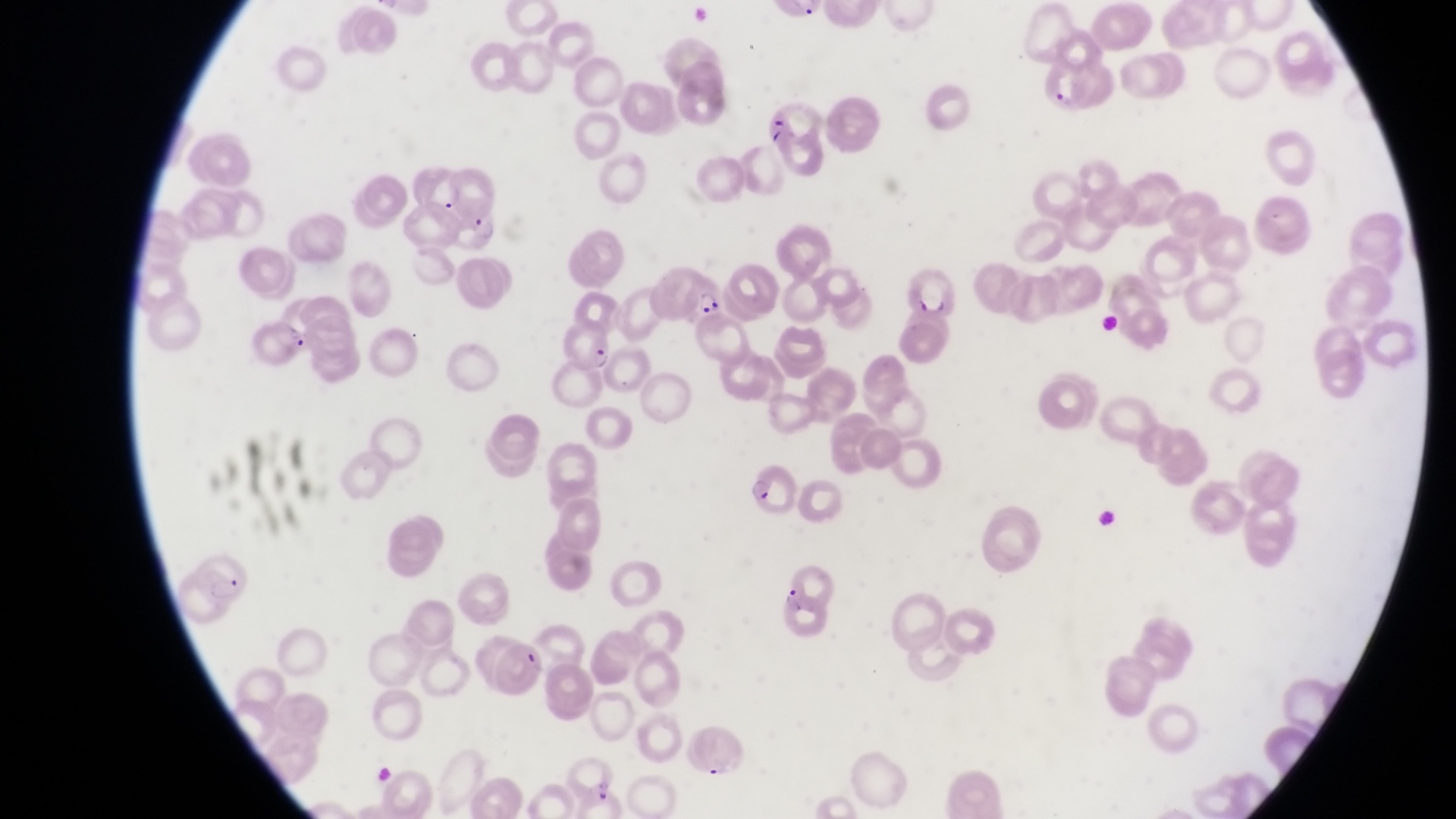 Approximate bounding boxes as {left, top, right, bottom} in pixels. Parasitised red blood cell locations: {444, 202, 504, 254}, {661, 262, 725, 320}, {901, 264, 960, 316}, {253, 312, 313, 365}, {561, 320, 617, 375}, {748, 462, 797, 520}, {184, 544, 261, 610}, {777, 582, 830, 641}, {682, 724, 750, 778}. Collected in Uganda. Image is 1456×819 pixels. Photographed through the eyepiece of an Olympus CX-23 microscope with a smartphone camera. Single field of view. Magnification of 1000x. Thin blood smear.